Report the malaria status of this cell.
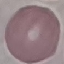

Uninfected.

Summary:
  - Image type: cell patch, automatically extracted from a larger field of view and resized to 64 × 64 pixels
  - Capture: smartphone through the microscope eyepiece
  - Stain: Giemsa
  - Preparation: thin blood film